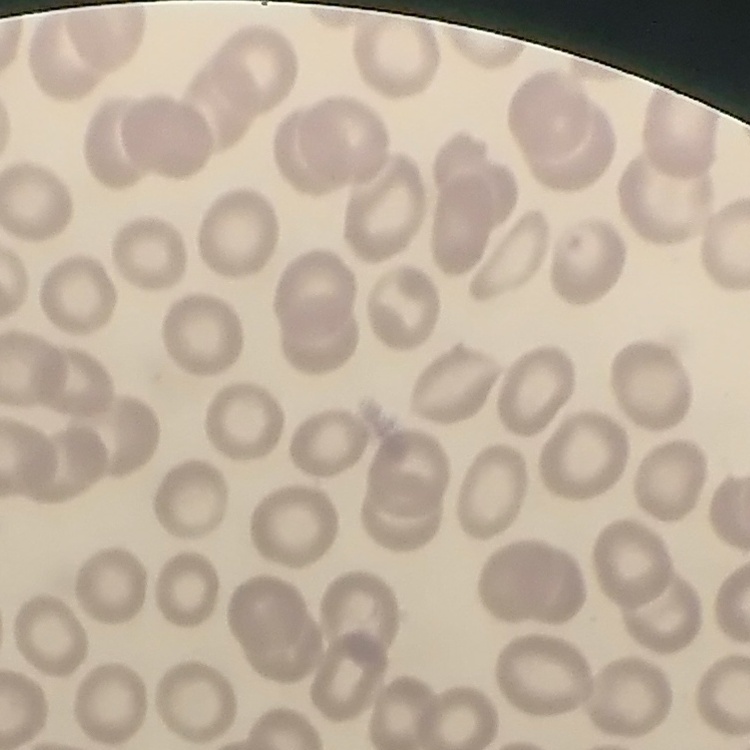

erythrocyte_morphology: no rouleaux formation
image_type: square crop of a larger photomicrograph
stain: Field's or Giemsa
preparation: thin blood smear